Give the position of every Plasmodium parasite visible.
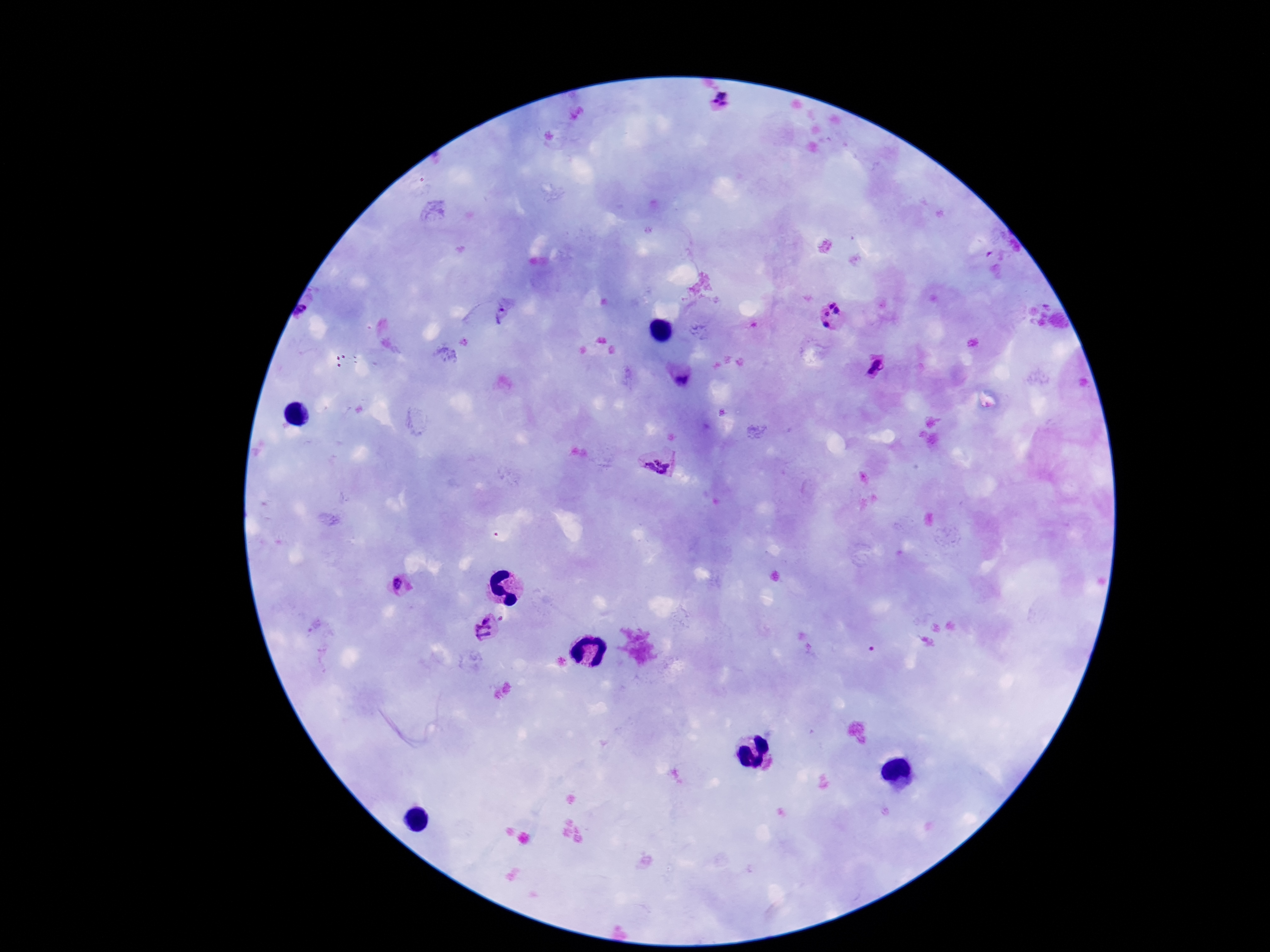
Approximate object centers, in pixels from the top-left corner.
Plasmodium parasites: (x=721, y=103), (x=505, y=314), (x=832, y=317), (x=879, y=368), (x=682, y=378), (x=657, y=462), (x=403, y=586), (x=487, y=629).

{
  "image_size": "1270×952 pixels",
  "patient_malaria_status": "infected",
  "capture": "smartphone camera through the microscope eyepiece",
  "magnification": "100x",
  "field_of_view": "one from this slide",
  "stain": "Giemsa",
  "preparation": "thick blood smear"
}